Locate and identify every blood parasite.
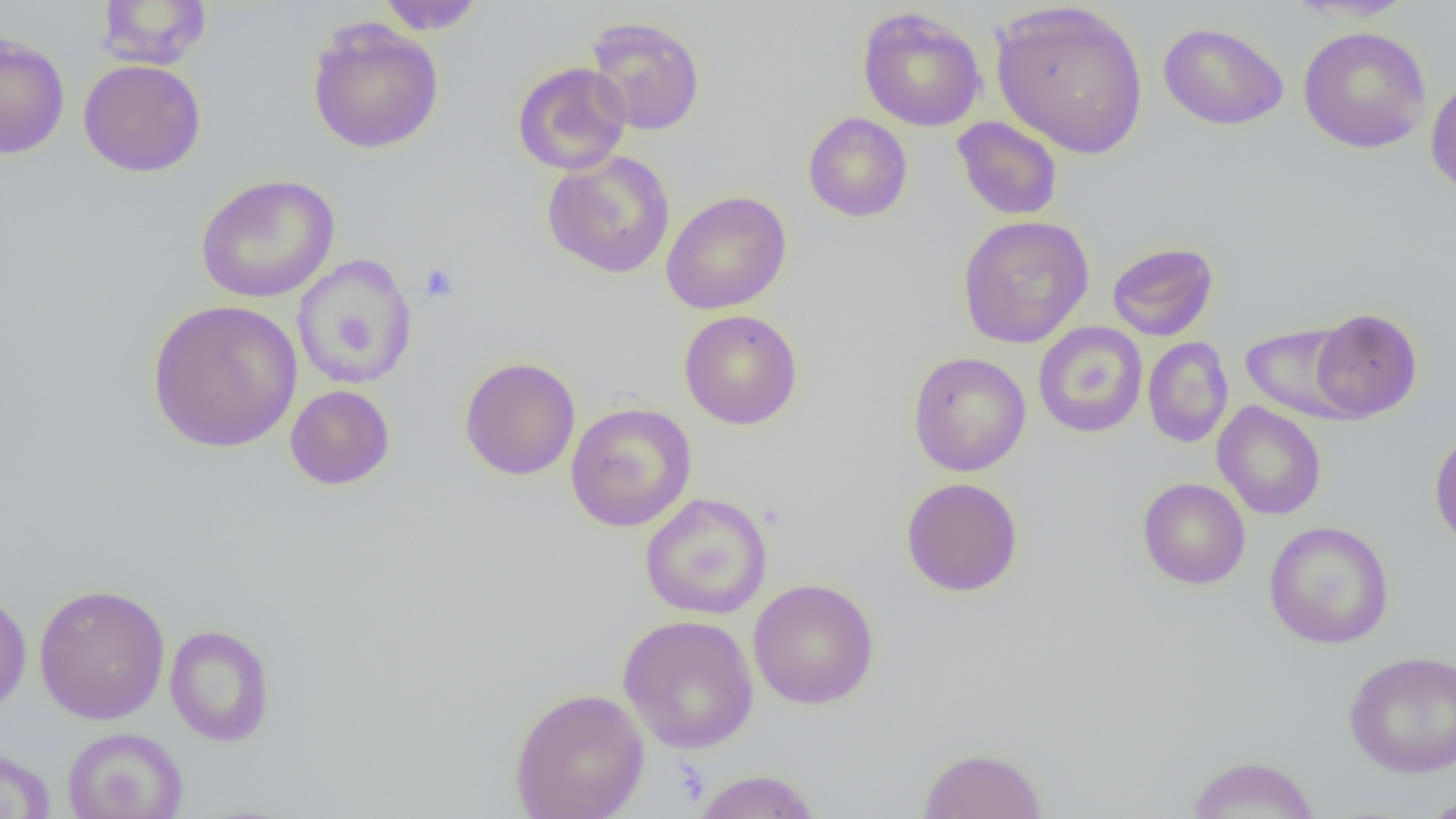
No blood parasites observed.

slide-level diagnosis = no evidence of blood parasites
uninfected red blood cell locations = approximate bounding boxes as (x1, y1, x2, y2) in pixels: (96, 0, 212, 70), (375, 0, 487, 34), (1287, 0, 1419, 22), (991, 1, 1149, 158), (857, 6, 987, 132), (584, 15, 705, 136), (306, 18, 445, 155), (1158, 21, 1289, 131), (1298, 26, 1432, 154), (0, 30, 70, 159), (78, 59, 206, 177), (512, 62, 632, 176), (1425, 74, 1456, 199), (803, 112, 913, 222), (952, 116, 1063, 220), (542, 151, 676, 278), (195, 174, 340, 303), (661, 190, 792, 315), (957, 215, 1094, 349), (1107, 242, 1218, 341), (292, 255, 417, 390), (147, 299, 303, 453), (1310, 308, 1423, 422), (679, 309, 803, 430), (1033, 321, 1148, 438), (1240, 322, 1363, 423), (1142, 337, 1233, 448), (907, 351, 1031, 476), (459, 357, 581, 480), (285, 384, 395, 490), (1212, 401, 1327, 520), (565, 402, 697, 532), (1429, 425, 1456, 552), (901, 477, 1023, 597), (1138, 477, 1250, 589), (640, 492, 772, 619), (1264, 520, 1394, 649), (748, 578, 880, 709), (33, 583, 171, 725), (0, 589, 31, 716), (618, 614, 759, 754), (164, 624, 275, 746), (1343, 650, 1456, 779), (509, 687, 650, 819), (62, 727, 188, 819), (0, 746, 57, 819), (917, 747, 1048, 818), (1186, 754, 1321, 818), (691, 769, 822, 819), (1419, 790, 1456, 818)
platelet locations = approximate bounding boxes as (x1, y1, x2, y2) in pixels: (419, 262, 458, 303)
image size = 1456×819 pixels
preparation = thin blood smear
magnification = 1000x
field of view = one of a larger specimen
modality = light microscopy